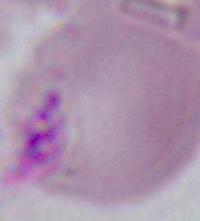

identification = erythrocyte
modality = photomicrograph
magnification = 1000x